State which cell type is depicted.
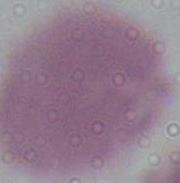

An erythrocyte.

{
  "magnification": "1000x",
  "modality": "photomicrograph"
}